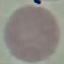 Malaria status: uninfected. Thin smear of blood. Automatically extracted cell patch, resized to 64 × 64 pixels. Giemsa-stained preparation. Acquired by smartphone through the microscope eyepiece.